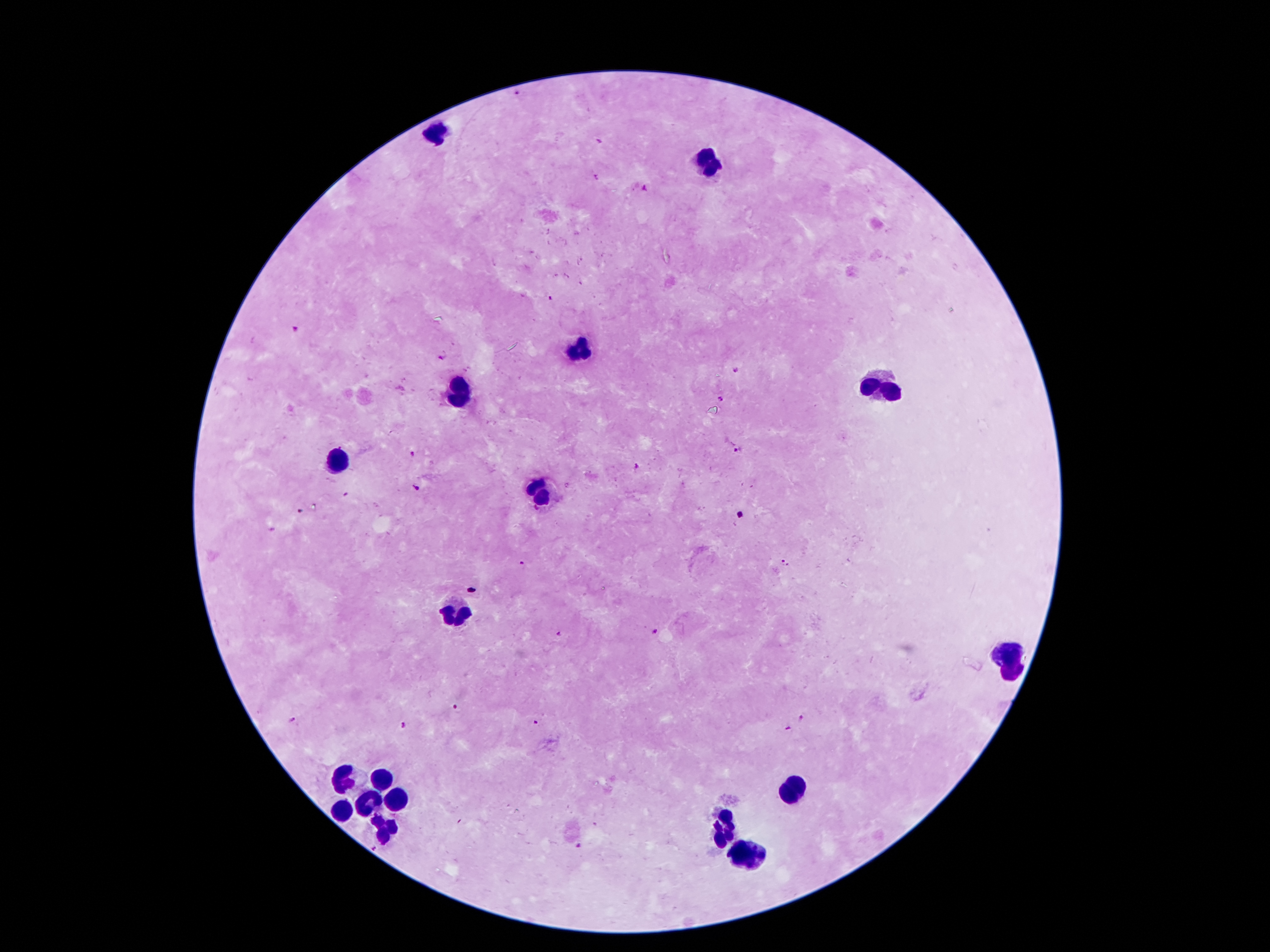

Approximate object centers, in pixels from the top-left corner.
Summary:
  - Leukocyte locations: (x=440, y=134), (x=707, y=160), (x=582, y=350), (x=882, y=387), (x=460, y=392), (x=339, y=463), (x=539, y=492), (x=455, y=611), (x=1009, y=658), (x=345, y=779), (x=384, y=780), (x=791, y=791), (x=393, y=795), (x=371, y=804), (x=341, y=810), (x=384, y=828), (x=726, y=828), (x=750, y=855)
  - Malaria parasite locations: (x=516, y=93), (x=645, y=187), (x=550, y=300), (x=296, y=329), (x=443, y=356), (x=735, y=370), (x=721, y=398), (x=738, y=450), (x=413, y=454), (x=637, y=466), (x=416, y=487), (x=299, y=511), (x=740, y=516), (x=522, y=564), (x=784, y=564), (x=656, y=632), (x=559, y=633), (x=456, y=706), (x=802, y=717), (x=292, y=720), (x=537, y=722), (x=406, y=725), (x=788, y=728), (x=580, y=846), (x=374, y=848)
  - Field of view: single
  - Preparation: thick blood smear
  - Capture: smartphone through the microscope eyepiece
  - Magnification: 100x
  - Stain: Giemsa
  - Image size: 1270×952 pixels
  - Patient malaria status: infected with Plasmodium falciparum